Assess this cell for malaria.
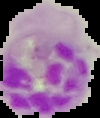
It is parasitized.

Image is 100×118 pixels. Cell region segmented out of the field of view; the surrounding area is masked to black. From a thin blood film.